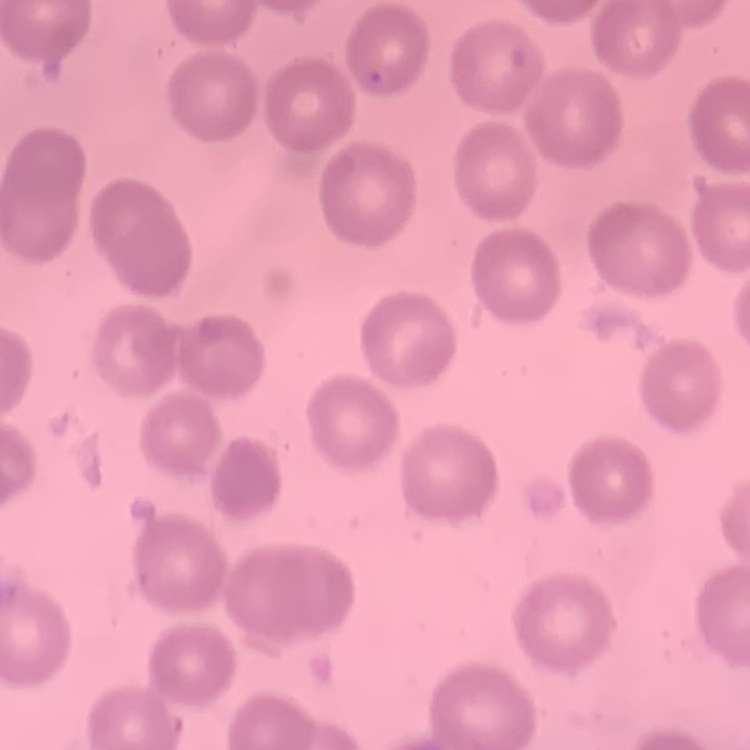

{
  "erythrocyte_morphology": "no rouleaux formation",
  "image_type": "square crop of a larger photomicrograph",
  "preparation": "thin blood film",
  "stain": "Field's or Giemsa"
}